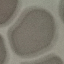
{
  "malaria_status": "uninfected",
  "preparation": "thin blood film",
  "image_type": "automatically extracted cell patch, resized to 64 × 64 pixels",
  "stain": "Giemsa",
  "capture": "smartphone through the microscope eyepiece"
}